State which parasite is depicted.
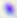

This is Toxoplasma gondii.

modality = photomicrograph
magnification = 400x